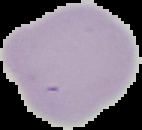

Summary:
  - Preparation: thin blood film
  - Image type: cell region segmented out of the field of view; surrounding area masked to black
  - Result: negative for Plasmodium parasites
  - Image size: 142×130 pixels